Locate every uninfected red blood cell.
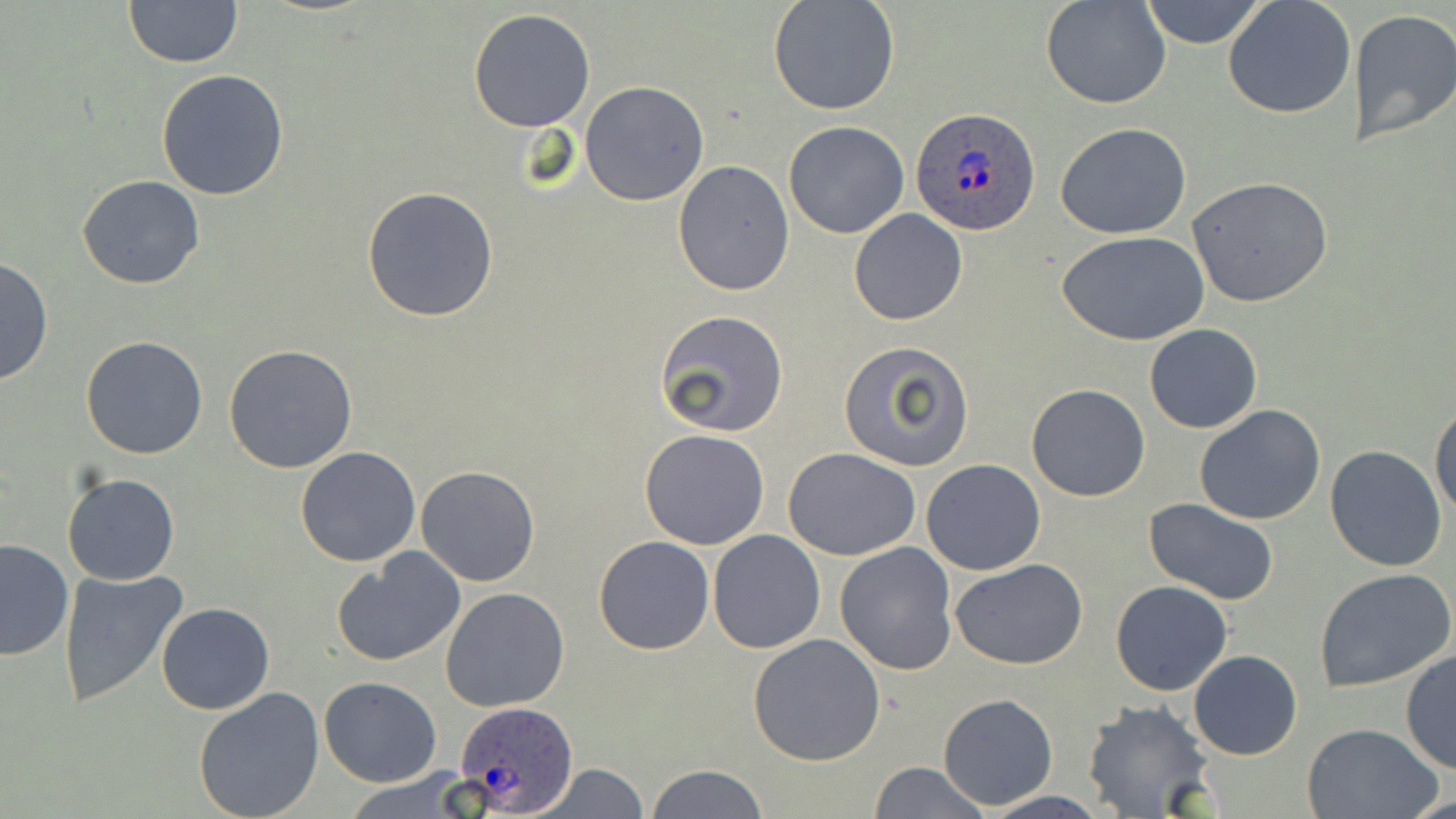

Approximate bounding boxes as named x1/y1/x2/y2 corners in pixels.
Uninfected red blood cells: (x1=122, y1=0, x2=243, y2=68), (x1=768, y1=0, x2=900, y2=116), (x1=1042, y1=0, x2=1169, y2=109), (x1=1138, y1=0, x2=1267, y2=48), (x1=1223, y1=0, x2=1356, y2=120), (x1=468, y1=7, x2=597, y2=132), (x1=1349, y1=9, x2=1456, y2=147), (x1=155, y1=68, x2=289, y2=201), (x1=580, y1=81, x2=710, y2=206), (x1=783, y1=120, x2=909, y2=239), (x1=1055, y1=123, x2=1191, y2=239), (x1=673, y1=160, x2=795, y2=296), (x1=78, y1=175, x2=204, y2=290), (x1=1187, y1=176, x2=1334, y2=307), (x1=362, y1=186, x2=499, y2=322), (x1=848, y1=208, x2=969, y2=327), (x1=1060, y1=231, x2=1210, y2=346), (x1=0, y1=258, x2=52, y2=386), (x1=654, y1=312, x2=789, y2=439), (x1=1145, y1=323, x2=1263, y2=433), (x1=80, y1=335, x2=209, y2=460), (x1=838, y1=340, x2=975, y2=470), (x1=223, y1=344, x2=359, y2=472), (x1=1025, y1=384, x2=1150, y2=502), (x1=1430, y1=401, x2=1456, y2=523), (x1=1194, y1=404, x2=1326, y2=526), (x1=639, y1=428, x2=770, y2=550), (x1=1325, y1=445, x2=1448, y2=571), (x1=296, y1=447, x2=422, y2=566), (x1=784, y1=448, x2=921, y2=562), (x1=920, y1=458, x2=1045, y2=575), (x1=415, y1=465, x2=541, y2=587), (x1=63, y1=471, x2=180, y2=586), (x1=1143, y1=498, x2=1280, y2=604), (x1=708, y1=528, x2=824, y2=652), (x1=592, y1=535, x2=715, y2=655), (x1=0, y1=538, x2=76, y2=661), (x1=834, y1=543, x2=960, y2=675), (x1=332, y1=549, x2=466, y2=667), (x1=951, y1=559, x2=1091, y2=670), (x1=58, y1=568, x2=189, y2=705), (x1=1315, y1=568, x2=1454, y2=691), (x1=1110, y1=580, x2=1233, y2=696), (x1=440, y1=587, x2=570, y2=712), (x1=154, y1=603, x2=274, y2=715), (x1=748, y1=633, x2=885, y2=766), (x1=1400, y1=649, x2=1456, y2=774), (x1=1188, y1=650, x2=1303, y2=760), (x1=319, y1=677, x2=442, y2=786), (x1=193, y1=688, x2=326, y2=819), (x1=938, y1=693, x2=1057, y2=810), (x1=1083, y1=699, x2=1218, y2=818), (x1=1302, y1=721, x2=1443, y2=818), (x1=537, y1=761, x2=650, y2=818), (x1=868, y1=761, x2=989, y2=819), (x1=644, y1=764, x2=768, y2=818), (x1=339, y1=770, x2=478, y2=819), (x1=977, y1=792, x2=1112, y2=819).

slide_level_diagnosis: Plasmodium ovale
field_of_view: single
magnification: 1000x
plasmodium_ovale_infected_red_blood_cell_locations: 'approximate bounding boxes as named x1/y1/x2/y2 corners in pixels: (x1=909, y1=107, x2=1041, y2=236), (x1=452, y1=702, x2=580, y2=812)'
image_size: 1456×819 pixels
stain: May-Grünwald-Giemsa
preparation: thin blood film
modality: optical microscopy